Name the parasite shown.
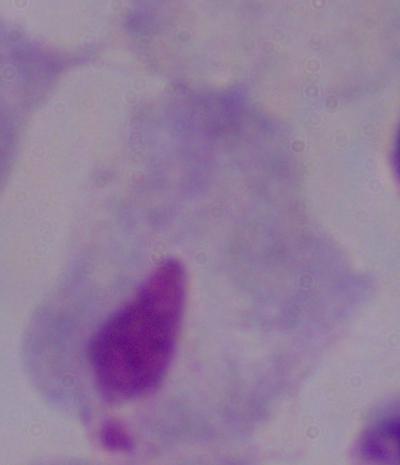

A trichomonad.

1000x magnification. Micrograph.